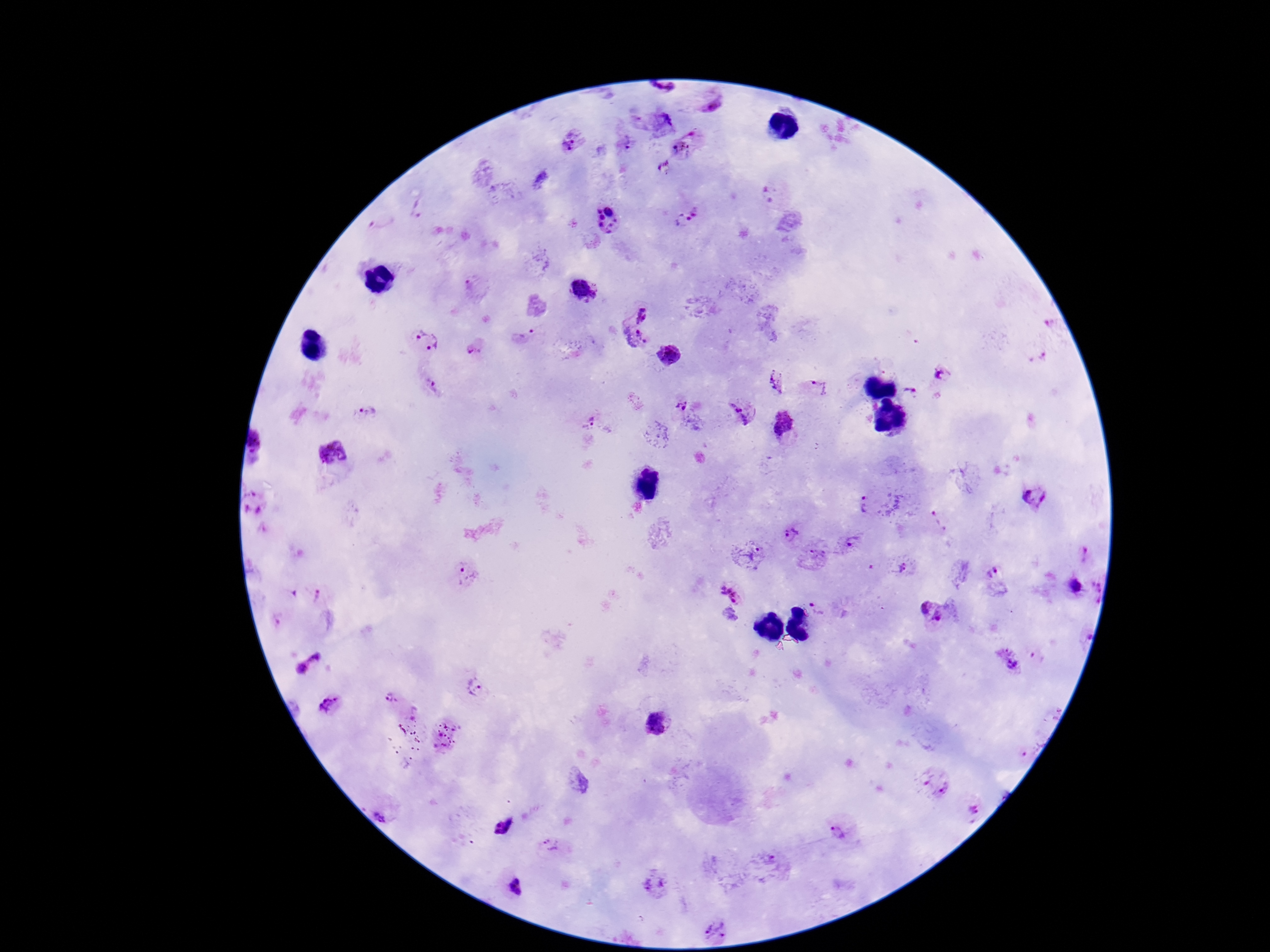
Approximate centers as [x, y] in pixels. Plasmodium parasite locations: [663, 89], [711, 108], [636, 122], [660, 123], [571, 140], [626, 144], [687, 144], [664, 170], [772, 195], [420, 209], [381, 218], [687, 218], [607, 222], [475, 288], [582, 291], [640, 312], [1048, 323], [526, 336], [635, 339], [425, 341], [476, 349], [670, 355], [1042, 356], [943, 375], [776, 380], [431, 385], [820, 387], [909, 394], [685, 402], [368, 411], [740, 414], [588, 422], [785, 425], [262, 447], [329, 455], [1034, 499], [255, 505], [866, 505], [937, 519], [788, 536], [849, 542], [1083, 553], [750, 557], [818, 558], [904, 567], [994, 574], [466, 575], [1075, 586], [1094, 591], [728, 594], [317, 595], [823, 607], [931, 611], [278, 620], [1082, 633], [1010, 660], [308, 664], [477, 688], [390, 699], [328, 701], [656, 722], [445, 736], [1029, 746], [936, 786], [385, 808], [970, 808], [504, 825], [839, 830], [551, 846], [772, 864], [655, 882], [516, 887], [716, 929]. Patient malaria status: positive. Giemsa stain. Smartphone photograph taken through the microscope eyepiece. Thick blood film. 100x magnification. Image is 1270×952 pixels. One field from this slide.